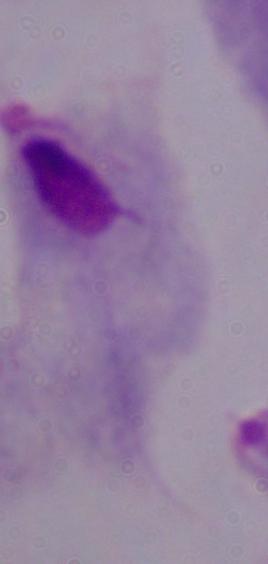 Photomicrograph. Captured at 1000x magnification. A trichomonad is shown.